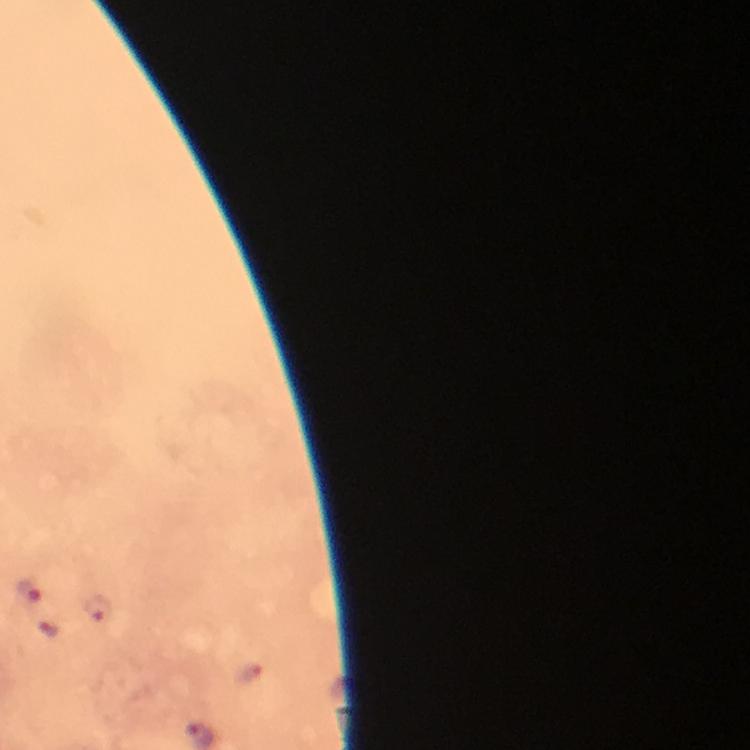
{
  "image_size": "750×750 pixels",
  "plasmodium_parasite_locations": "approximate centers as [x, y] in pixels: [29, 590], [96, 607]",
  "cropped_from": "a single field of view",
  "context": "from a malaria diagnostic workup",
  "preparation": "thick blood film",
  "magnification": "100x",
  "stain": "Giemsa",
  "immersion_oil": "applied",
  "capture": "smartphone photograph through a microscope"
}